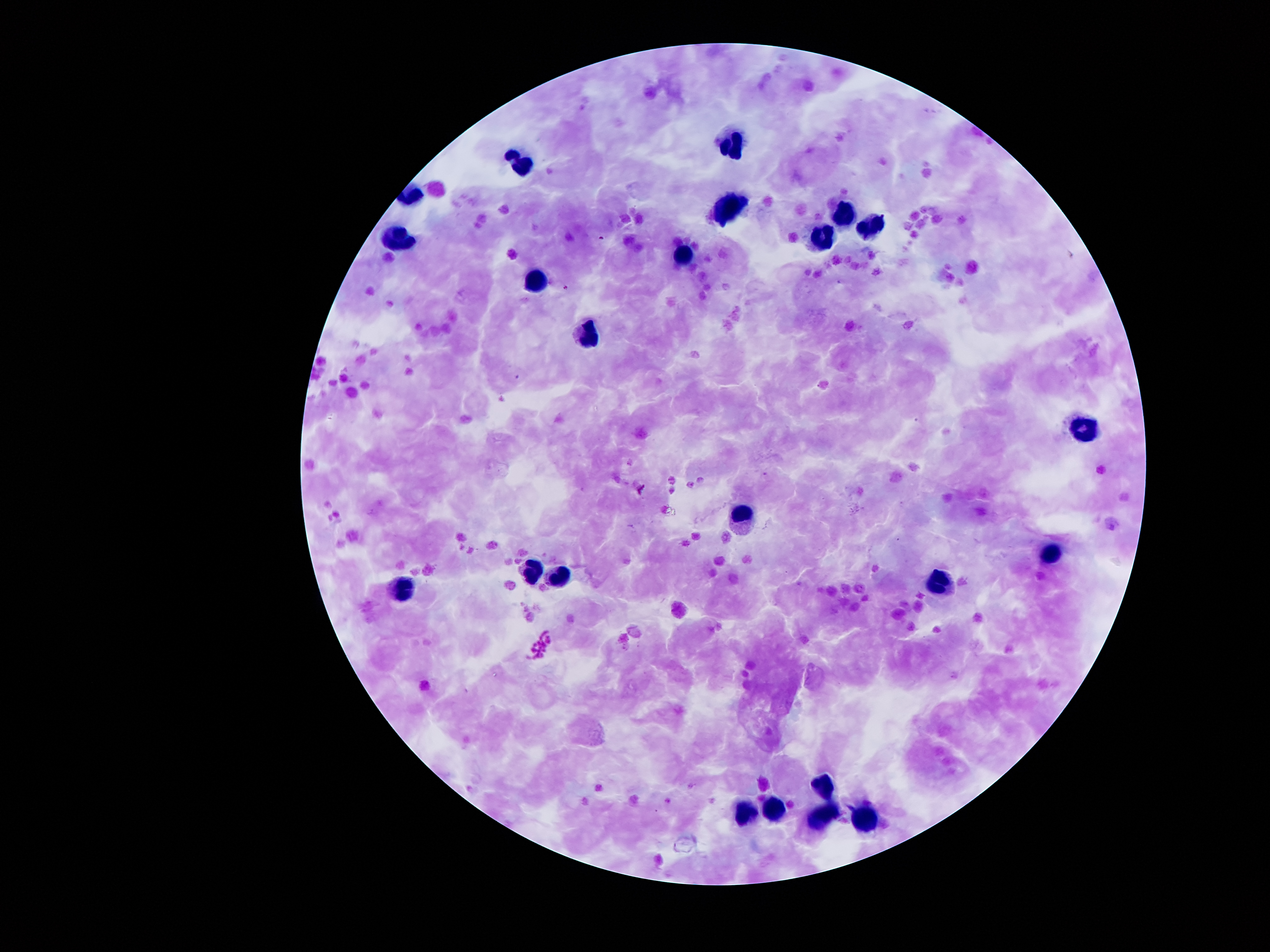

Approximate centers as {x, y} in pixels.
Summary:
  - Leukocyte locations: {733, 142}, {518, 165}, {735, 207}, {847, 216}, {871, 227}, {823, 239}, {401, 241}, {682, 253}, {535, 282}, {590, 339}, {1086, 426}, {742, 516}, {1054, 552}, {531, 570}, {559, 577}, {938, 583}, {400, 591}, {821, 783}, {776, 808}, {749, 814}, {825, 814}, {865, 817}
  - Malaria parasite locations: {602, 238}, {565, 288}, {765, 475}
  - Field of view: single
  - Preparation: thick blood film
  - Capture: smartphone camera through the microscope eyepiece
  - Patient malaria status: infected with Plasmodium falciparum
  - Image size: 1270×952 pixels
  - Magnification: 100x
  - Stain: Giemsa